Locate every Plasmodium parasite.
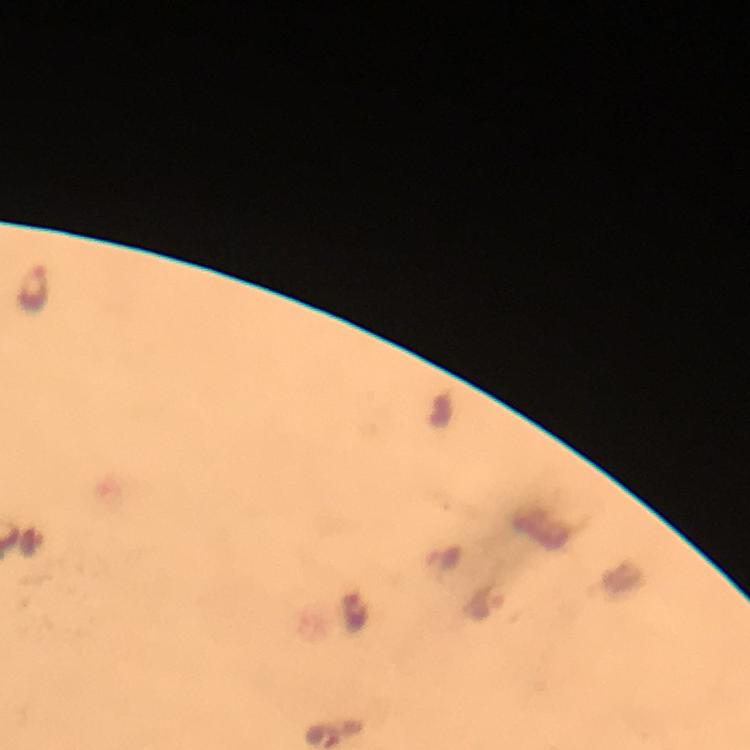
Approximate object centers, in pixels from the top-left corner.
Plasmodium parasites: (x=33, y=288), (x=442, y=560), (x=485, y=601), (x=354, y=610).

Summary:
  - Cropped from: a single field of view
  - Capture: smartphone camera through the microscope
  - Magnification: 100x
  - Image size: 750×750 pixels
  - Immersion oil: used
  - Preparation: thick smear
  - Stain: Giemsa
  - Context: from a malaria diagnostic workup